Assess this cell for malaria.
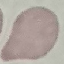
It is uninfected.

Summary:
  - Preparation: thin smear
  - Stain: Giemsa
  - Image type: cell patch, automatically extracted from a larger field of view and resized to 64 × 64 pixels
  - Capture: smartphone through the microscope eyepiece